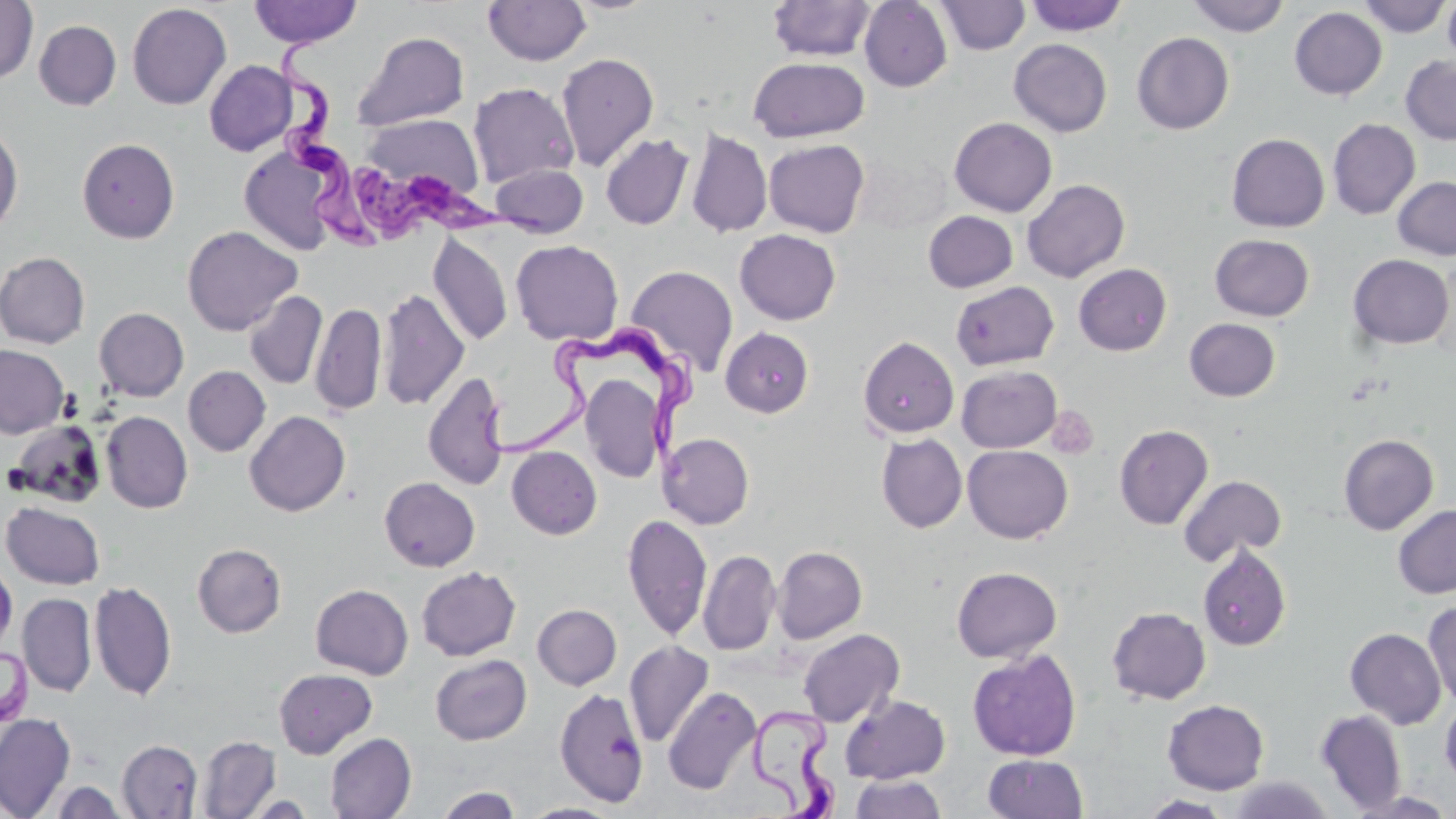 Approximate bounding boxes as [x1, y1, x2, y2] in pixels. Trypanosoma brucei locations: [272, 37, 385, 255], [346, 157, 546, 249], [477, 317, 696, 474], [748, 699, 845, 818]. Uninfected red blood cell locations: [0, 0, 38, 84], [249, 0, 362, 48], [1024, 0, 1129, 36], [1187, 0, 1290, 36], [1358, 0, 1450, 37], [1442, 0, 1456, 68], [482, 1, 592, 66], [768, 1, 875, 61], [859, 1, 952, 92], [935, 1, 1031, 55], [127, 3, 232, 110], [1289, 7, 1387, 99], [34, 20, 122, 110], [353, 31, 469, 130], [1132, 32, 1234, 134], [1009, 39, 1113, 136], [556, 52, 659, 171], [1400, 55, 1456, 144], [749, 56, 869, 142], [204, 60, 298, 156], [468, 82, 579, 188], [362, 113, 485, 198], [949, 117, 1057, 217], [1328, 118, 1420, 219], [0, 122, 24, 235], [687, 128, 772, 238], [600, 133, 694, 229], [1227, 133, 1329, 232], [77, 138, 179, 243], [764, 139, 870, 237], [239, 145, 339, 255], [853, 152, 951, 234], [489, 163, 588, 238], [1392, 176, 1456, 260], [1021, 179, 1130, 282], [923, 210, 1018, 292], [182, 225, 302, 335], [734, 229, 841, 325], [428, 232, 513, 347], [1210, 234, 1314, 321], [511, 239, 624, 345], [0, 252, 90, 349], [1348, 253, 1454, 350], [1073, 263, 1172, 355], [626, 264, 739, 376], [951, 280, 1059, 370], [377, 287, 469, 411], [244, 291, 327, 389], [311, 302, 386, 415], [94, 307, 189, 401], [1184, 318, 1280, 401], [721, 327, 814, 417], [858, 336, 959, 438], [0, 344, 69, 438], [957, 365, 1062, 453], [183, 366, 270, 456], [422, 370, 510, 491], [580, 372, 666, 483], [244, 410, 351, 516], [102, 411, 193, 513], [6, 420, 108, 508], [1114, 424, 1213, 529], [659, 433, 754, 529], [1339, 433, 1439, 534], [876, 434, 967, 533], [962, 445, 1073, 543], [507, 446, 602, 539], [1179, 474, 1287, 566], [379, 477, 480, 572], [2, 501, 105, 589], [1393, 504, 1456, 599], [623, 513, 712, 641], [192, 543, 286, 637], [1198, 545, 1292, 651], [772, 546, 867, 644], [698, 549, 781, 655], [0, 557, 17, 658], [416, 566, 521, 661], [951, 566, 1061, 663], [89, 580, 177, 702], [310, 584, 413, 679], [18, 593, 96, 696], [1423, 601, 1456, 709], [533, 604, 621, 689], [1107, 606, 1211, 705], [1345, 627, 1447, 729], [798, 629, 904, 727], [624, 640, 714, 747], [0, 645, 33, 730], [967, 649, 1082, 761], [430, 654, 532, 745], [274, 668, 378, 758], [663, 686, 760, 794], [554, 688, 649, 808], [841, 695, 950, 784], [1162, 699, 1270, 795], [1440, 700, 1456, 789], [1315, 709, 1406, 814], [0, 712, 76, 818], [325, 733, 416, 819], [197, 735, 280, 818], [117, 739, 202, 818], [983, 753, 1089, 819], [851, 775, 947, 819], [1227, 776, 1336, 818], [50, 780, 128, 818], [434, 786, 523, 818], [1140, 794, 1233, 818], [520, 802, 621, 819]. Platelet locations: [1047, 406, 1099, 460]. Slide-level diagnosis: Trypanosoma brucei. Thin blood smear. Captured at 1000x magnification. May-Grünwald-Giemsa stain. Image is 1456×819 pixels. One field of a larger specimen. Light microscopy.